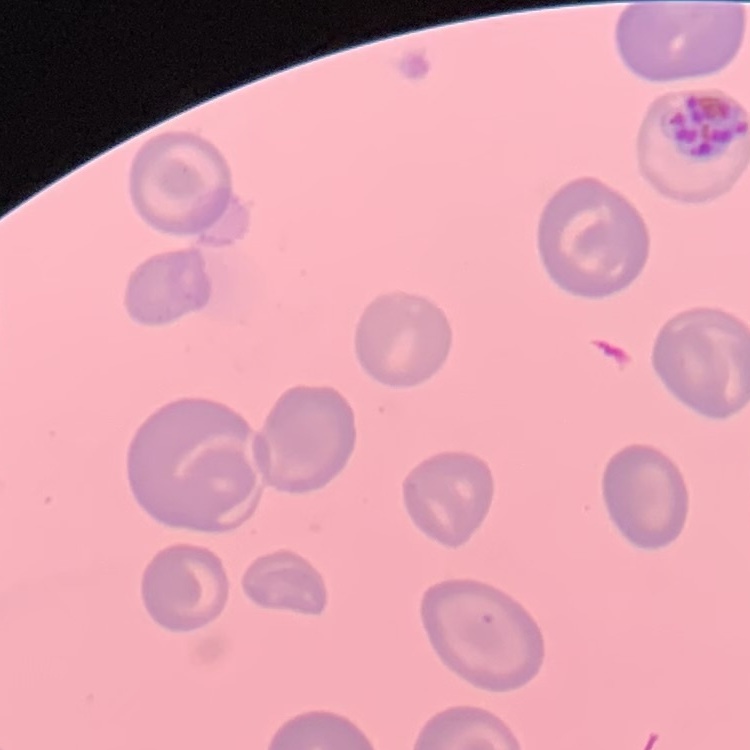
Summary:
  - Erythrocyte morphology: no rouleaux formation
  - Preparation: thin blood smear
  - Stain: Field's or Giemsa
  - Image type: square crop of a larger photomicrograph